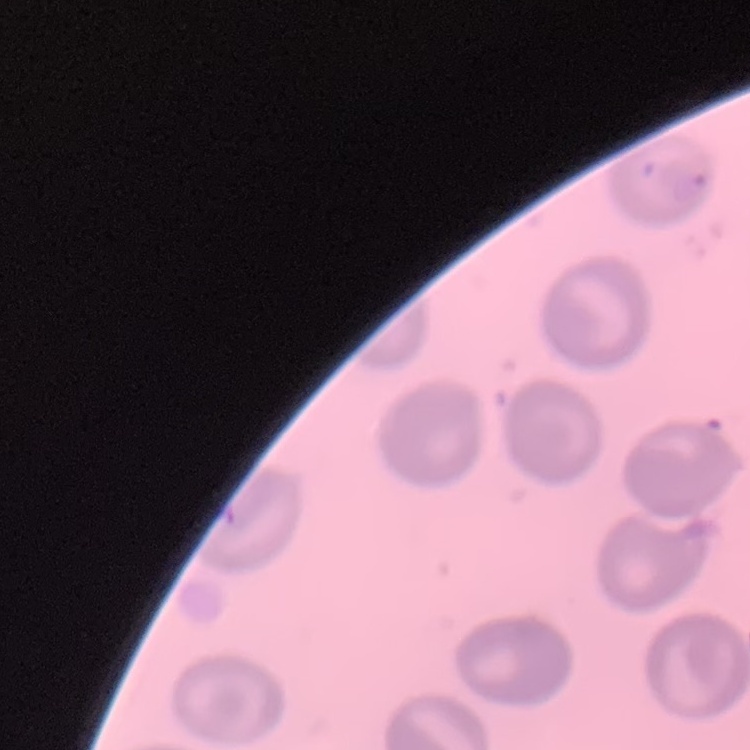

The erythrocytes show no rouleaux formation. Square crop of a larger photomicrograph. Field's or Giemsa stain. Thin blood film.